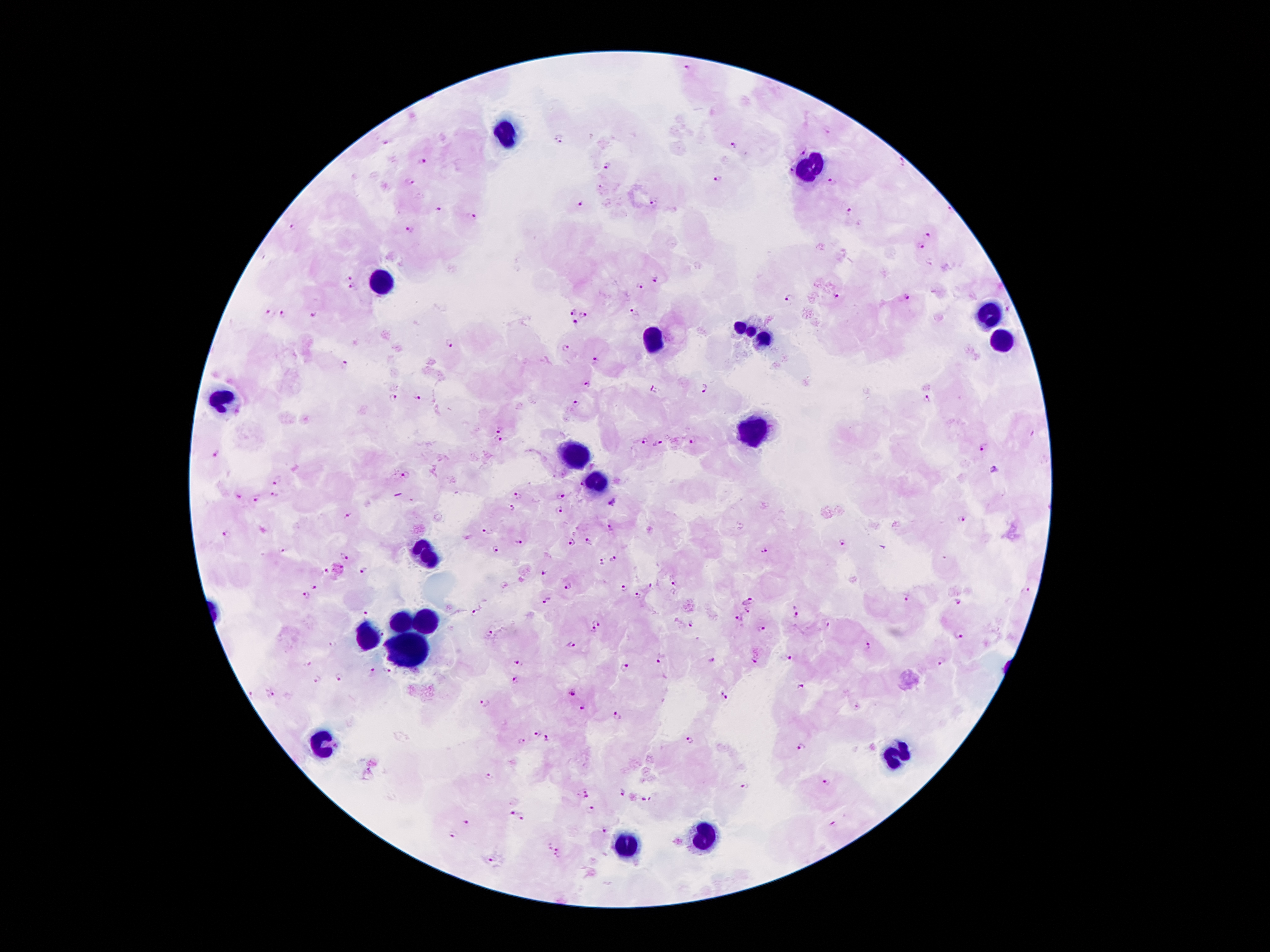 Approximate centers as {x, y} in pixels. Leukocyte locations: {506, 134}, {812, 170}, {381, 282}, {987, 315}, {749, 334}, {651, 343}, {1000, 343}, {222, 400}, {753, 429}, {576, 454}, {594, 482}, {424, 555}, {403, 620}, {422, 623}, {363, 635}, {408, 650}, {326, 741}, {898, 754}, {701, 839}, {624, 847}. Plasmodium parasite locations: {828, 133}, {559, 139}, {383, 142}, {733, 145}, {803, 153}, {423, 162}, {901, 165}, {608, 167}, {788, 170}, {717, 180}, {831, 181}, {410, 182}, {582, 203}, {654, 203}, {438, 210}, {848, 211}, {470, 218}, {293, 226}, {411, 229}, {928, 236}, {919, 246}, {347, 278}, {656, 279}, {353, 287}, {640, 287}, {835, 296}, {907, 297}, {788, 301}, {269, 312}, {631, 312}, {573, 313}, {315, 314}, {284, 315}, {585, 315}, {575, 323}, {448, 342}, {566, 349}, {595, 360}, {346, 365}, {589, 386}, {705, 389}, {654, 390}, {420, 396}, {394, 398}, {929, 401}, {575, 404}, {501, 428}, {643, 440}, {692, 440}, {497, 441}, {657, 444}, {982, 448}, {217, 454}, {993, 471}, {404, 476}, {277, 483}, {580, 484}, {275, 495}, {560, 495}, {519, 496}, {239, 497}, {255, 500}, {612, 503}, {513, 509}, {558, 511}, {347, 517}, {961, 518}, {611, 526}, {486, 530}, {224, 534}, {519, 540}, {589, 541}, {569, 542}, {843, 545}, {496, 549}, {285, 550}, {764, 551}, {344, 557}, {612, 558}, {600, 560}, {324, 571}, {364, 572}, {545, 574}, {568, 585}, {676, 585}, {623, 588}, {651, 588}, {314, 589}, {1028, 591}, {639, 595}, {305, 596}, {905, 598}, {749, 600}, {956, 600}, {548, 601}, {747, 609}, {798, 610}, {365, 613}, {476, 613}, {740, 618}, {692, 624}, {828, 625}, {762, 629}, {594, 630}, {489, 633}, {958, 636}, {572, 644}, {334, 645}, {869, 647}, {788, 657}, {661, 659}, {714, 660}, {514, 662}, {756, 662}, {941, 662}, {307, 665}, {624, 668}, {389, 671}, {373, 673}, {340, 678}, {316, 679}, {515, 681}, {801, 686}, {572, 692}, {269, 693}, {723, 695}, {486, 703}, {582, 707}, {856, 708}, {616, 717}, {538, 732}, {547, 738}, {522, 740}, {690, 741}, {803, 748}, {489, 776}, {827, 784}, {745, 785}, {623, 793}, {587, 795}, {646, 800}, {592, 807}, {513, 815}, {521, 818}, {466, 822}, {837, 824}, {605, 830}, {453, 834}, {559, 849}, {556, 858}, {490, 862}. Patient malaria status: positive for Plasmodium falciparum. Thick blood smear. Single field of view. Giemsa-stained preparation. Smartphone photograph taken through the microscope eyepiece. Image is 1270×952 pixels. 100x magnification.